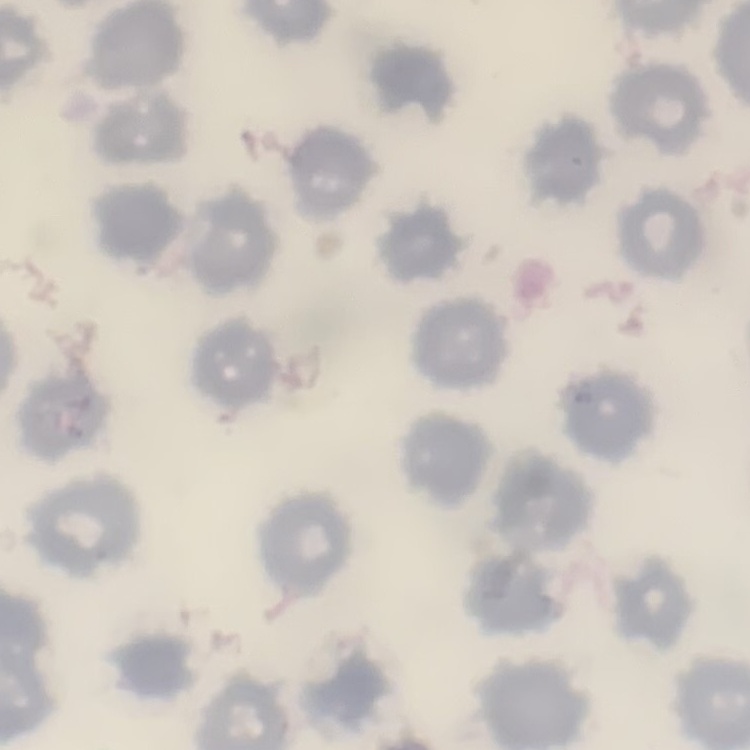

Summary:
  - Red blood cell morphology: no rouleaux formation
  - Stain: Field's or Giemsa
  - Image type: one tile cut from a larger photomicrograph
  - Preparation: thin peripheral smear